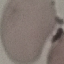

Summary:
  - Malaria status: uninfected
  - Stain: Giemsa
  - Capture: smartphone camera at the microscope eyepiece
  - Preparation: thin smear
  - Image type: automatically extracted cell patch, resized to 64 × 64 pixels